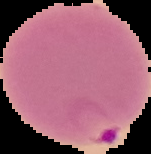

Summary:
  - Result: Plasmodium parasites detected
  - Image type: segmented cell region with the area outside set to black
  - Image size: 151×154 pixels
  - Preparation: thin blood smear